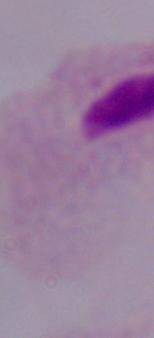 Photomicrograph. 1000x magnification. A trichomonad is shown.